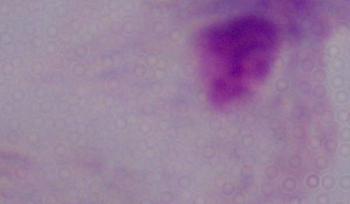
Summary:
  - Magnification: 1000x
  - Modality: photomicrograph
  - Identification: trichomonad